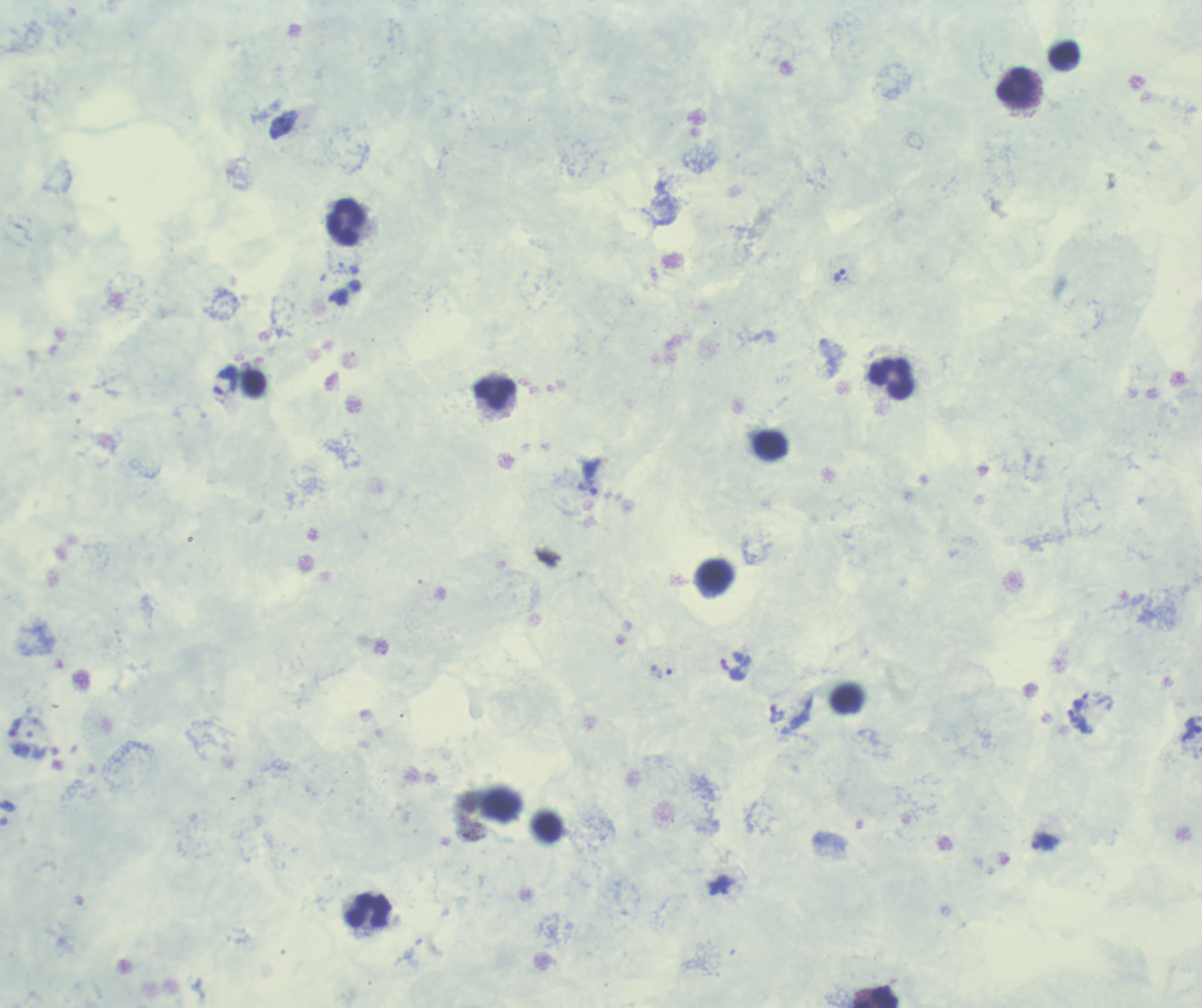
Approximate centers as {x, y} in pixels.
Summary:
  - Trophozoite locations: {839, 276}, {338, 297}, {225, 379}, {587, 476}, {662, 672}, {1079, 715}, {1045, 841}, {721, 887}
  - Leukocyte locations: {1064, 55}, {1016, 86}, {346, 222}, {891, 379}, {494, 394}, {770, 445}, {715, 575}, {369, 910}, {876, 997}
  - Result: positive for Plasmodium parasites
  - Background quality: poor
  - Field of view: single
  - Image size: 1202×1008 pixels
  - Magnification: 100x
  - Stain: Romanowsky
  - Preparation: thick smear of blood
  - Context: previously used in an actual diagnosis